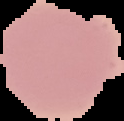
Summary:
  - Result: no malaria parasites detected
  - Preparation: thin blood film
  - Image size: 124×121 pixels
  - Image type: segmented cell region with the area outside set to black